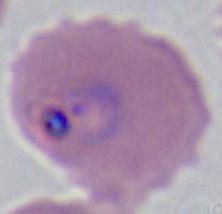

Summary:
  - Identification: Plasmodium
  - Modality: micrograph
  - Magnification: 400x or 1000x